Describe the morphology of the erythrocytes.
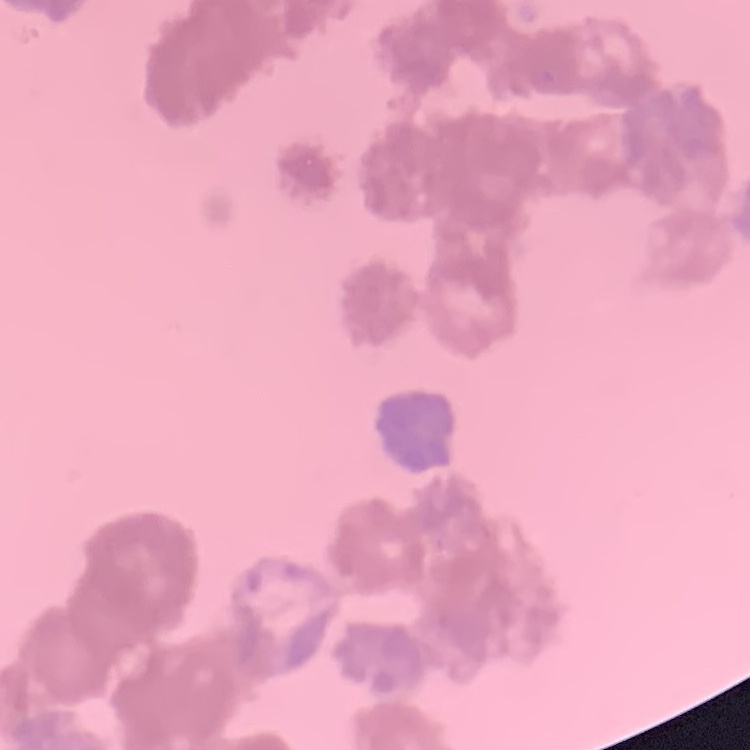

Rouleaux formation.

preparation: thin blood film
stain: Field's or Giemsa
image_type: one tile cut from a larger photomicrograph